Outline each uninfected red blood cell.
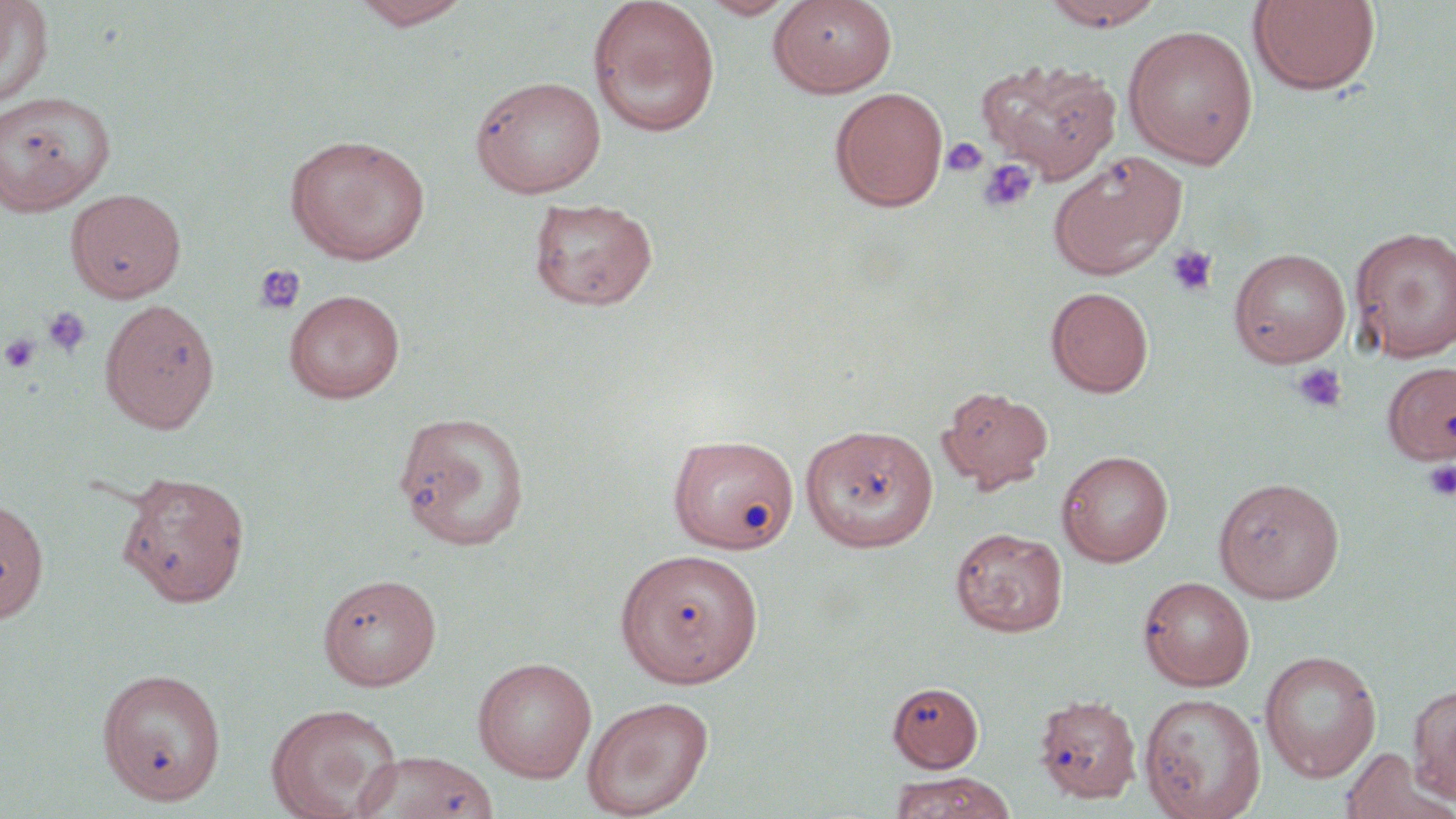

Approximate bounding boxes as named x1/y1/x2/y2 corners in pixels.
Uninfected red blood cells: (x1=0, y1=0, x2=54, y2=108), (x1=350, y1=0, x2=473, y2=30), (x1=587, y1=0, x2=722, y2=137), (x1=699, y1=0, x2=800, y2=20), (x1=768, y1=0, x2=897, y2=96), (x1=1041, y1=0, x2=1166, y2=30), (x1=1247, y1=1, x2=1382, y2=96), (x1=1123, y1=25, x2=1259, y2=168), (x1=975, y1=58, x2=1122, y2=183), (x1=470, y1=75, x2=607, y2=198), (x1=829, y1=87, x2=949, y2=212), (x1=0, y1=90, x2=116, y2=216), (x1=284, y1=133, x2=432, y2=265), (x1=1048, y1=150, x2=1188, y2=279), (x1=65, y1=188, x2=186, y2=303), (x1=528, y1=196, x2=659, y2=311), (x1=1350, y1=226, x2=1456, y2=362), (x1=1228, y1=247, x2=1351, y2=367), (x1=1046, y1=286, x2=1154, y2=398), (x1=283, y1=289, x2=405, y2=403), (x1=99, y1=298, x2=220, y2=435), (x1=1384, y1=361, x2=1456, y2=464), (x1=938, y1=386, x2=1053, y2=492), (x1=393, y1=409, x2=532, y2=551), (x1=799, y1=422, x2=938, y2=552), (x1=668, y1=433, x2=800, y2=553), (x1=1057, y1=449, x2=1174, y2=567), (x1=116, y1=470, x2=251, y2=607), (x1=1212, y1=477, x2=1345, y2=603), (x1=0, y1=497, x2=49, y2=624), (x1=950, y1=527, x2=1068, y2=637), (x1=615, y1=548, x2=764, y2=688), (x1=317, y1=572, x2=442, y2=690), (x1=1137, y1=575, x2=1255, y2=691), (x1=1259, y1=650, x2=1381, y2=782), (x1=472, y1=657, x2=598, y2=782), (x1=97, y1=667, x2=227, y2=806), (x1=887, y1=681, x2=984, y2=772), (x1=1408, y1=683, x2=1455, y2=804), (x1=1034, y1=693, x2=1141, y2=803), (x1=1138, y1=693, x2=1266, y2=819), (x1=582, y1=695, x2=713, y2=818), (x1=265, y1=702, x2=403, y2=819), (x1=1339, y1=747, x2=1452, y2=819), (x1=354, y1=751, x2=500, y2=819), (x1=889, y1=772, x2=1014, y2=819).

Summary:
  - Platelet locations: (x1=941, y1=137, x2=989, y2=179), (x1=977, y1=158, x2=1038, y2=215), (x1=1165, y1=244, x2=1219, y2=297), (x1=252, y1=263, x2=306, y2=315), (x1=42, y1=307, x2=91, y2=357), (x1=0, y1=333, x2=42, y2=374), (x1=1291, y1=362, x2=1348, y2=413), (x1=1423, y1=460, x2=1456, y2=501)
  - Slide-level diagnosis: negative for blood parasites
  - Modality: light microscopy
  - Preparation: thin blood film
  - Stain: May-Grünwald-Giemsa
  - Magnification: 1000x
  - Image size: 1456×819 pixels
  - Field of view: one of a larger specimen